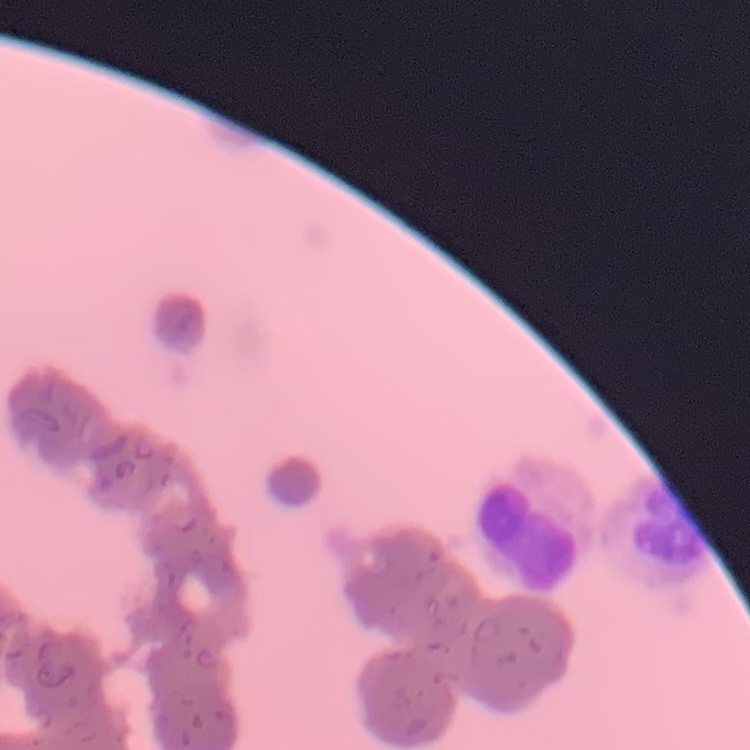
The erythrocytes show rouleaux formation. One tile cut from a larger photomicrograph. Thin blood smear. Field's or Giemsa stain.